Assess this cell for malaria.
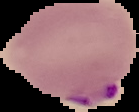
Parasitized.

image_size: 139×112 pixels
preparation: thin blood smear
image_type: cell region segmented out of the field of view; surrounding area masked to black